Outline platelets.
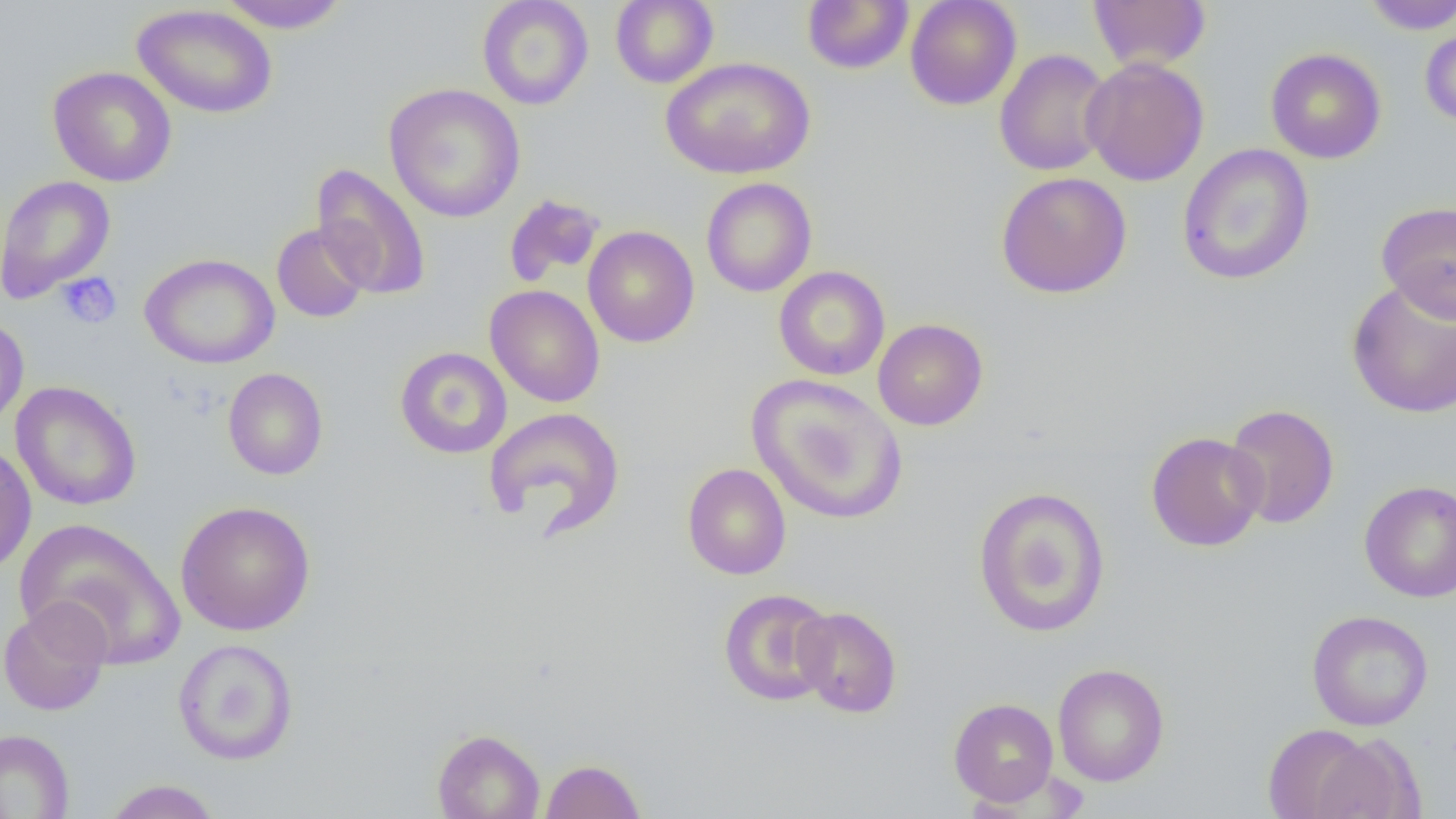
Approximate bounding boxes as (x1,y1)-(x2,y2) corner pairs in pixels.
Platelets: (56,271)-(122,329).

Uninfected red blood cell locations: (214,0)-(351,33), (477,0)-(594,110), (610,0)-(719,88), (802,0)-(914,74), (905,0)-(1022,110), (1088,0)-(1211,72), (1360,1)-(1456,34), (132,4)-(277,119), (1420,20)-(1456,129), (995,48)-(1113,176), (1266,48)-(1386,164), (661,57)-(816,180), (1081,57)-(1209,186), (47,66)-(177,187), (384,83)-(525,223), (1177,143)-(1315,286), (311,161)-(431,301), (995,172)-(1132,298), (0,175)-(115,303), (701,177)-(817,297), (503,194)-(606,288), (1376,200)-(1456,322), (271,223)-(372,323), (583,225)-(699,348), (140,253)-(279,369), (774,265)-(890,380), (1346,277)-(1456,420), (485,285)-(605,407), (0,315)-(29,430), (873,318)-(988,430), (395,346)-(512,459), (223,368)-(328,480), (748,374)-(907,525), (11,381)-(141,511), (1223,403)-(1340,529), (483,407)-(625,536), (1145,431)-(1268,552), (0,443)-(37,575), (682,463)-(792,579), (1359,480)-(1456,603), (972,486)-(1111,638), (175,500)-(315,635), (14,518)-(185,668), (718,588)-(836,706), (0,599)-(112,717), (793,606)-(902,718), (1306,610)-(1433,731), (173,638)-(299,765), (1052,662)-(1169,787), (948,697)-(1059,805), (1261,722)-(1385,818), (0,728)-(75,818), (432,728)-(545,819), (1306,731)-(1425,819), (541,758)-(646,818), (103,779)-(222,819). Slide-level diagnosis: negative for blood parasites. Thin blood film. Single field of view. 1000x magnification. Image is 1456×819 pixels. Optical microscopy.